Give the preparation type.
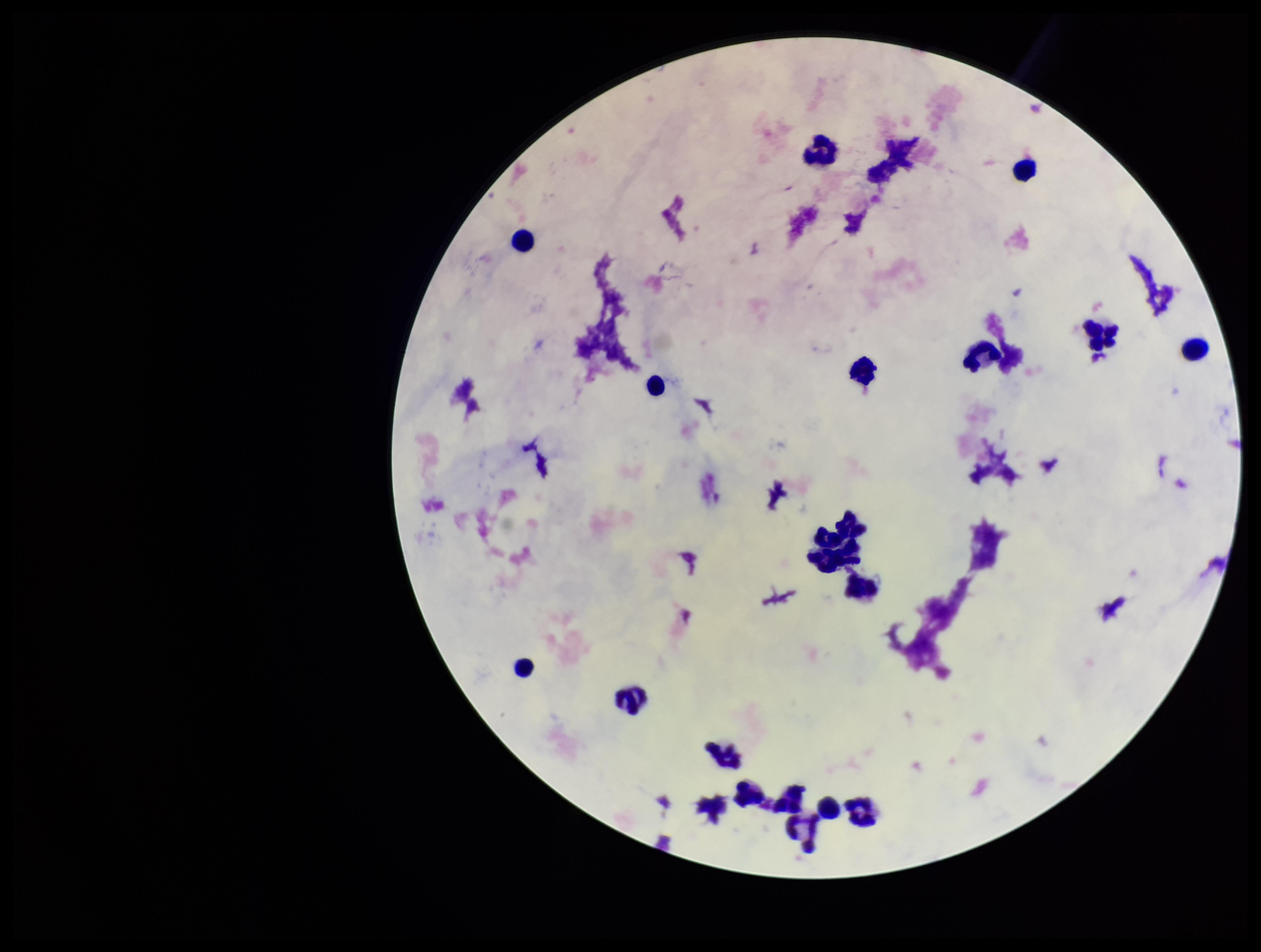
A thick smear.

Summary:
  - Field of view: one from this slide
  - Patient malaria status: negative
  - Image size: 1261×952 pixels
  - Leukocyte count: 20
  - Plasmodium parasites: none seen
  - Parasite count: 0
  - Stain: Giemsa
  - Capture: smartphone photograph through the microscope eyepiece